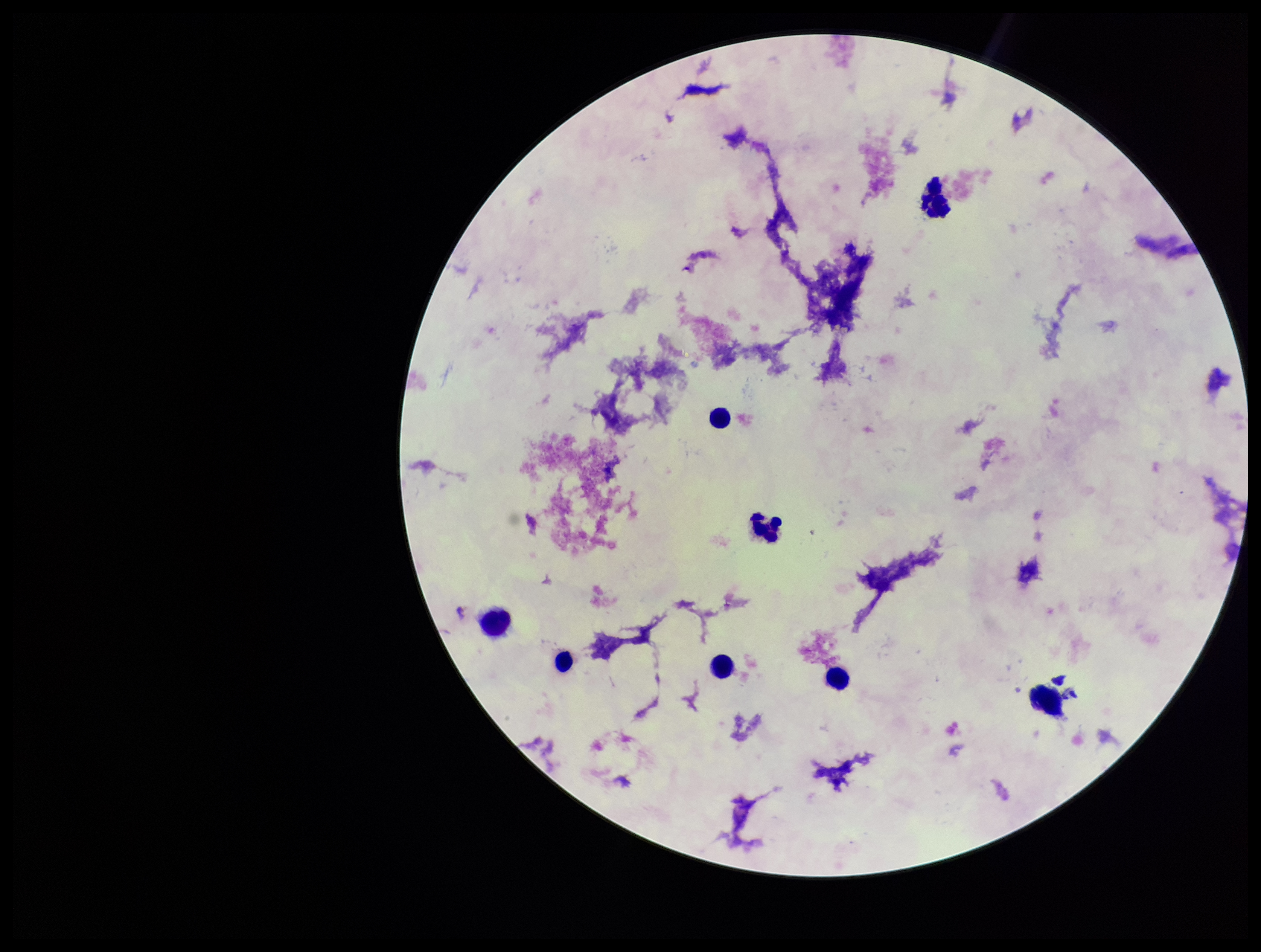
Summary:
  - Stain: Giemsa
  - Preparation: thick blood smear
  - Plasmodium parasites: none seen
  - Parasite count: 0
  - Capture: smartphone photograph through the microscope eyepiece
  - Leukocyte count: 7
  - Image size: 1261×952 pixels
  - Patient malaria status: negative
  - Field of view: one from this slide